Comment on the morphology of the erythrocytes.
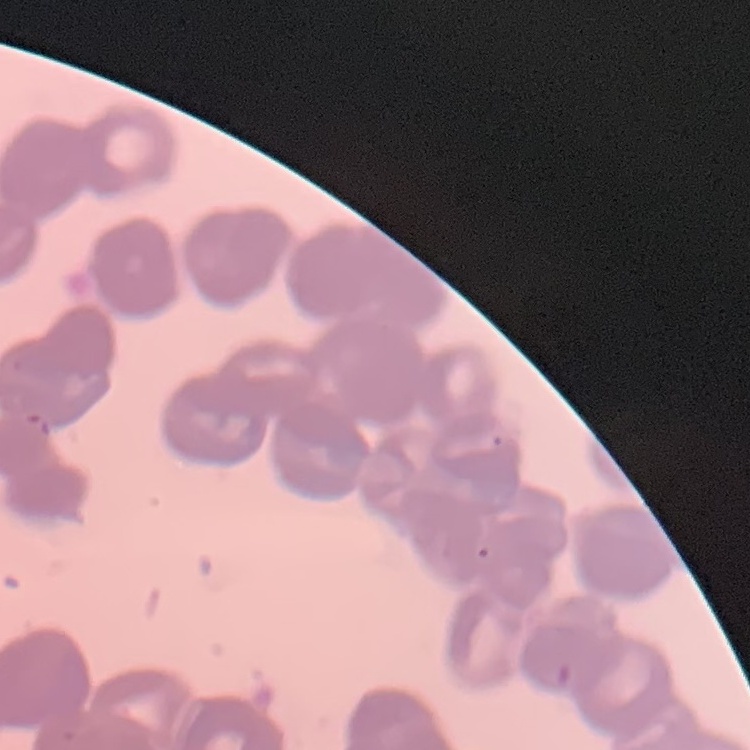
Rouleaux formation.

Stained with either Field's or Giemsa. Thin blood film. One tile cut from a larger photomicrograph.